Comment on the morphology of the erythrocytes.
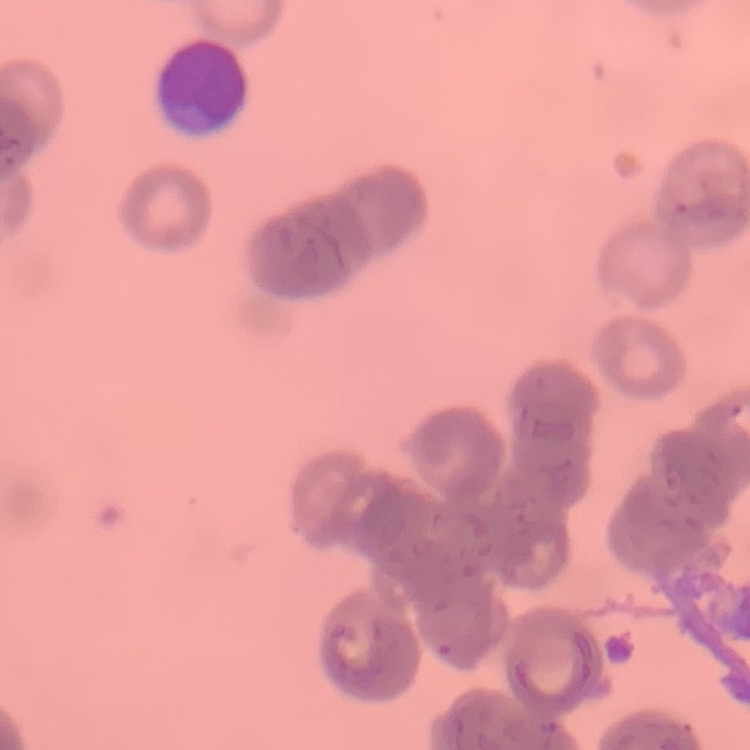

Rouleaux formation.

stain: Field's or Giemsa
preparation: thin blood film
image_type: one tile cut from a larger photomicrograph